Point out each leukocyte.
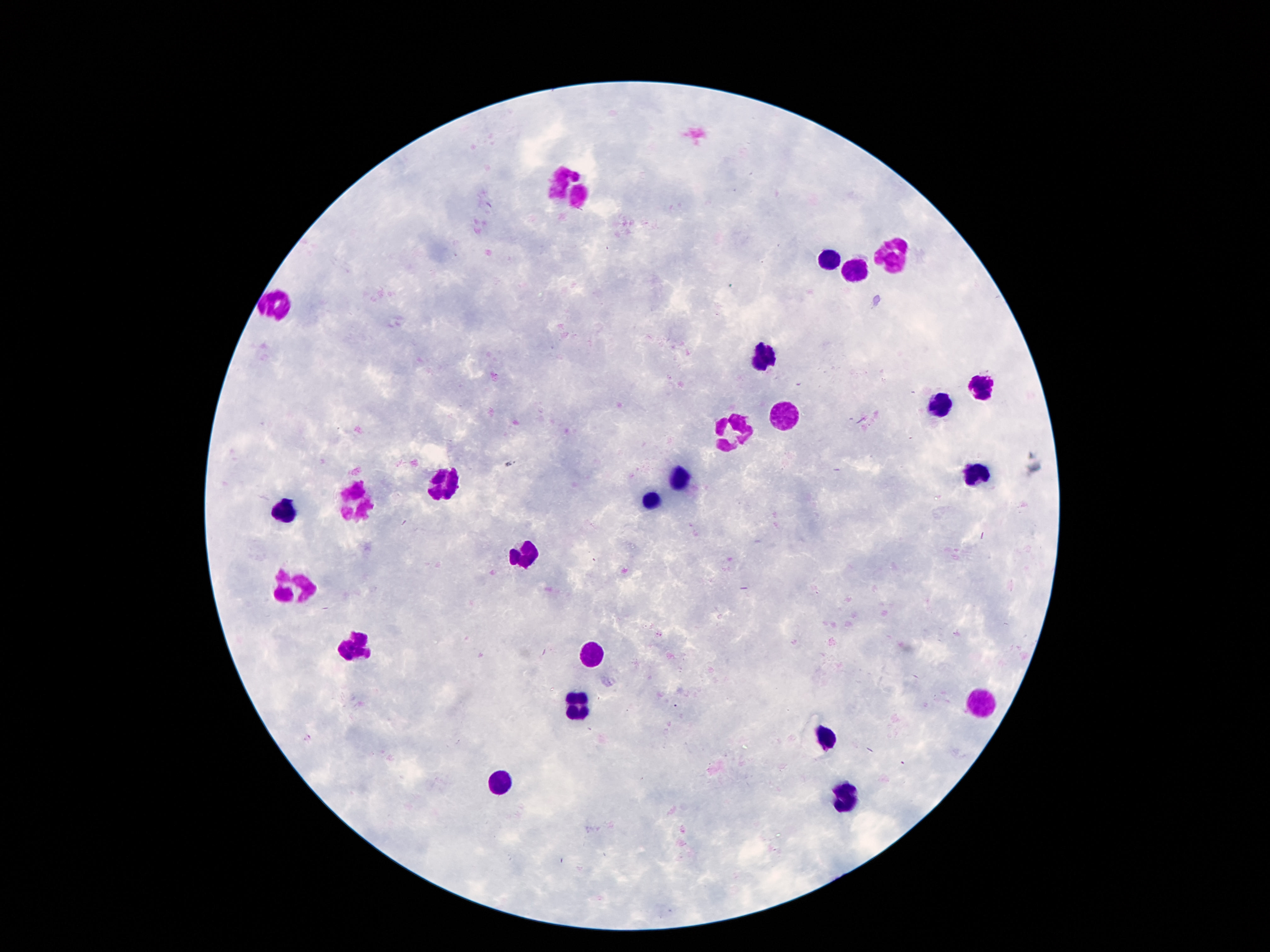
Approximate centers as [x, y] in pixels.
Leukocytes: [569, 188], [896, 255], [827, 260], [862, 266], [276, 303], [765, 356], [976, 389], [941, 403], [788, 422], [728, 430], [976, 475], [683, 479], [438, 485], [354, 500], [651, 502], [286, 512], [526, 555], [292, 590], [358, 647], [593, 655], [577, 700], [980, 706], [827, 737], [505, 782], [845, 798].

Summary:
  - Stain: Giemsa
  - Capture: smartphone camera through the microscope eyepiece
  - Preparation: thick peripheral-blood smear
  - Magnification: 100x
  - Field of view: single
  - Image size: 1270×952 pixels
  - Patient malaria status: uninfected